State the blood parasite species.
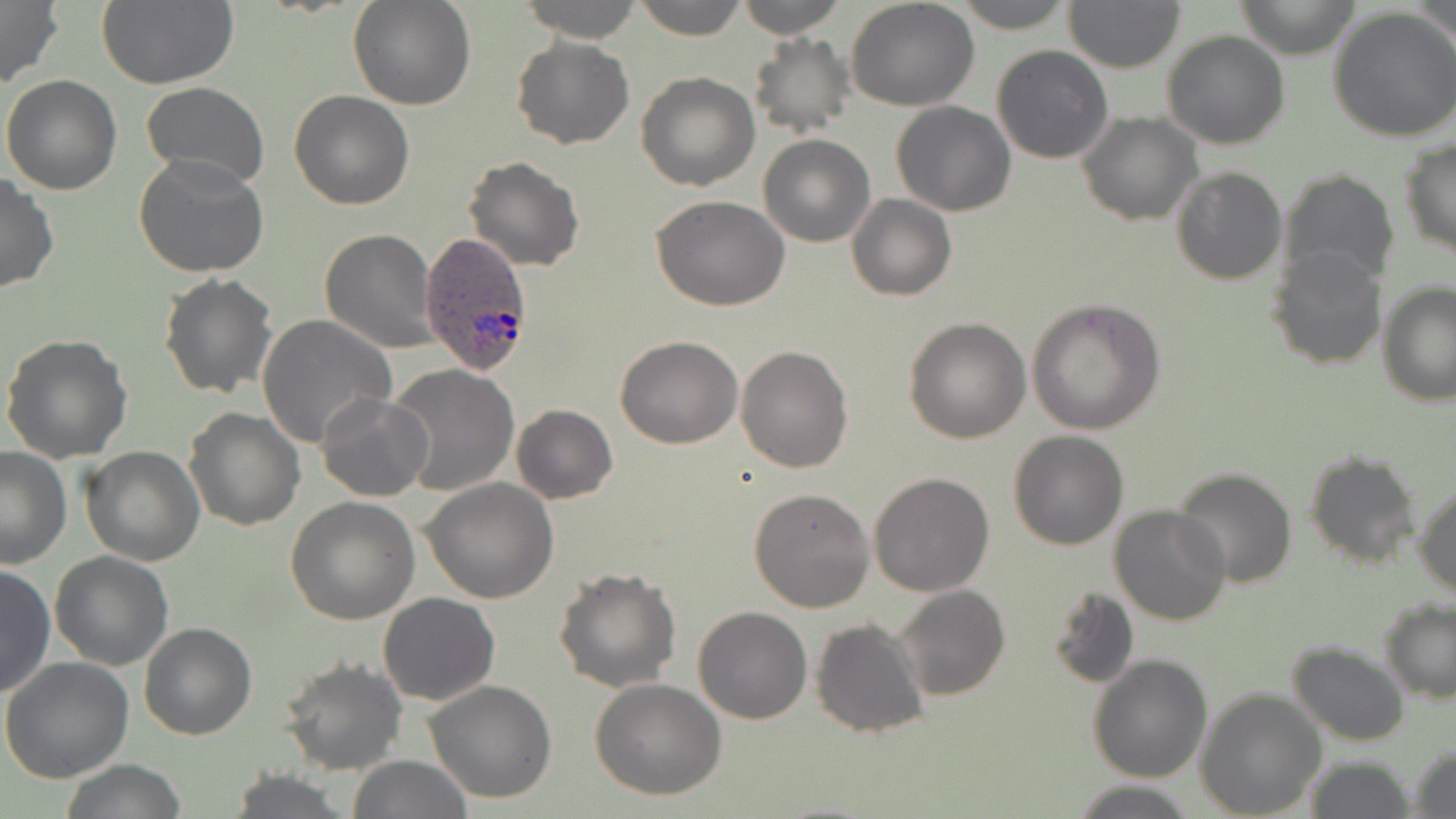
Plasmodium ovale.

Summary:
  - Coordinate format: approximate bounding boxes as [x1, y1, x2, y2] in pixels
  - Uninfected red blood cell locations: [347, 0, 476, 112], [515, 0, 644, 44], [631, 0, 749, 40], [733, 0, 851, 38], [953, 0, 1075, 30], [1062, 0, 1185, 72], [1233, 0, 1360, 59], [1413, 0, 1455, 45], [0, 1, 63, 87], [847, 1, 981, 111], [96, 2, 238, 89], [1328, 7, 1456, 142], [1162, 31, 1290, 149], [748, 34, 857, 141], [511, 36, 635, 149], [991, 45, 1114, 164], [636, 72, 760, 191], [2, 73, 123, 194], [141, 81, 270, 188], [288, 89, 415, 209], [892, 102, 1017, 217], [1077, 112, 1202, 225], [759, 135, 874, 246], [1399, 138, 1456, 256], [135, 154, 270, 278], [463, 155, 584, 271], [1171, 165, 1289, 284], [1280, 169, 1400, 288], [0, 173, 59, 294], [847, 194, 956, 300], [650, 196, 791, 312], [321, 229, 439, 353], [1266, 243, 1392, 371], [159, 272, 276, 399], [1378, 283, 1455, 408], [1026, 297, 1168, 434], [257, 314, 397, 450], [904, 316, 1032, 443], [1, 334, 133, 463], [614, 335, 743, 449], [736, 344, 853, 473], [388, 364, 520, 495], [316, 393, 435, 502], [510, 403, 619, 503], [184, 407, 306, 532], [1008, 430, 1128, 549], [0, 446, 73, 569], [79, 447, 205, 565], [1303, 450, 1421, 570], [1171, 468, 1297, 588], [869, 472, 995, 596], [421, 478, 560, 605], [1412, 483, 1456, 598], [748, 486, 875, 611], [286, 496, 420, 625], [1110, 506, 1232, 625], [50, 551, 173, 670], [0, 563, 55, 700], [554, 566, 680, 692], [1044, 583, 1140, 692], [894, 584, 1009, 702], [379, 592, 499, 706], [1380, 600, 1456, 703], [693, 606, 812, 725], [810, 618, 928, 738], [139, 622, 256, 741], [1288, 642, 1411, 746], [1087, 654, 1212, 784], [278, 657, 407, 774], [0, 658, 133, 783], [591, 677, 727, 801], [425, 680, 557, 803], [1194, 687, 1327, 817], [1408, 744, 1456, 818], [347, 755, 474, 819], [1301, 755, 1415, 819], [60, 760, 187, 818], [228, 769, 353, 819], [1070, 780, 1199, 819]
  - Plasmodium ovale-infected red blood cell locations: [419, 233, 536, 374]
  - Modality: light microscopy
  - Image size: 1456×819 pixels
  - Field of view: one of a larger specimen
  - Stain: May-Grünwald-Giemsa
  - Magnification: 1000x
  - Preparation: thin blood film